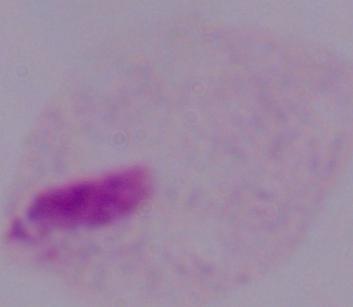

A trichomonad is seen. Captured at 1000x magnification. Photomicrograph.